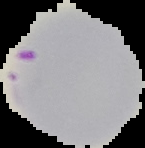
Summary:
  - Preparation: thin blood film
  - Image type: cell region segmented out of the field of view; surrounding area masked to black
  - Result: malaria parasites identified
  - Image size: 145×148 pixels